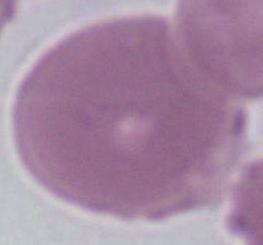 Micrograph. 1000x magnification. A red blood cell is shown.